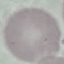

Summary:
  - Result: no malaria parasites seen
  - Preparation: thin blood smear
  - Stain: Giemsa
  - Image type: cell patch, automatically extracted from a larger field of view and resized to 64 × 64 pixels
  - Capture: smartphone camera at the microscope eyepiece